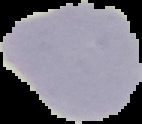
image size = 142×124 pixels
malaria status = uninfected
image type = segmented cell region on a black background
preparation = thin blood film